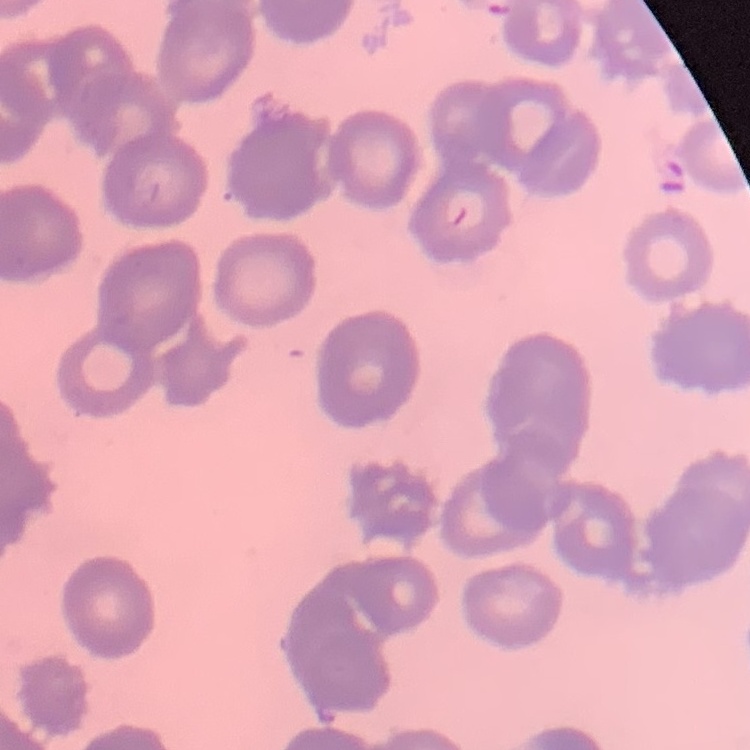
Summary:
  - Red blood cell morphology: rouleaux formation
  - Stain: Field's or Giemsa
  - Image type: one tile cut from a larger photomicrograph
  - Preparation: thin peripheral smear